Name the cell type shown.
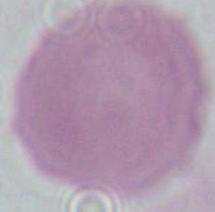
This is an erythrocyte.

Summary:
  - Magnification: 1000x
  - Modality: photomicrograph